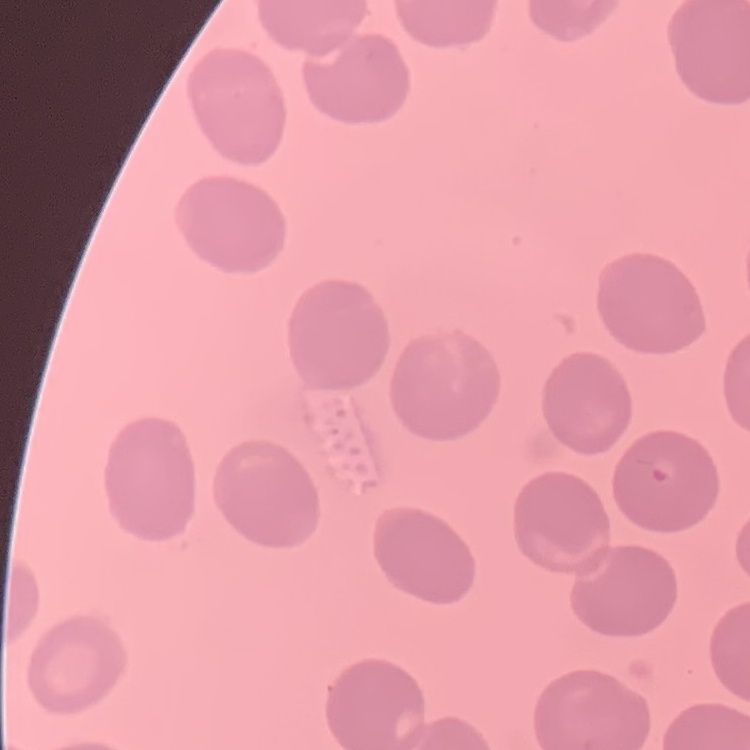

erythrocyte_morphology: no rouleaux formation
stain: Field's or Giemsa
preparation: thin peripheral smear
image_type: square crop of a larger photomicrograph